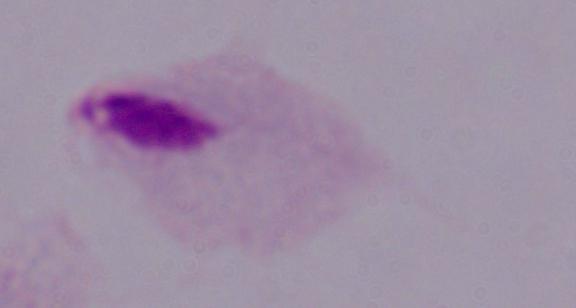
Micrograph. A trichomonad is shown. 1000x magnification.